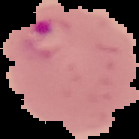

preparation: thin blood smear
result: Plasmodium parasites detected
image_type: segmented cell region with the area outside set to black
image_size: 139×139 pixels